Classify the preparation.
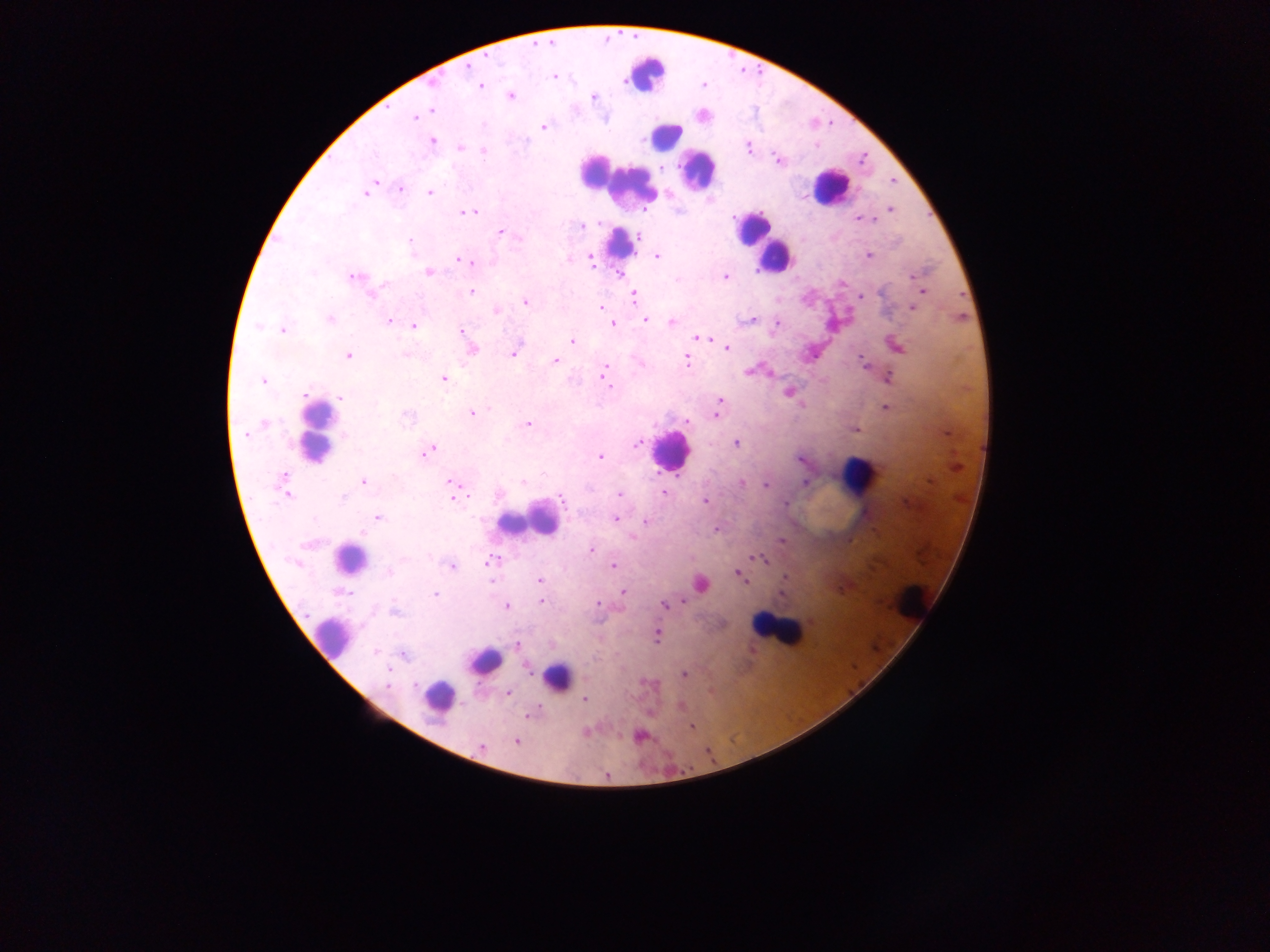

Thick blood smear.

Approximate centers as (x, y) in pixels.
Summary:
  - Malaria parasite locations: (487, 58), (467, 66), (554, 76), (624, 81), (434, 83), (704, 85), (480, 86), (510, 96), (594, 97), (431, 110), (420, 114), (415, 117), (543, 127), (433, 142), (460, 147), (748, 148), (483, 150), (777, 160), (663, 168), (893, 181), (401, 189), (366, 193), (430, 193), (891, 210), (470, 213), (866, 219), (582, 226), (500, 232), (639, 235), (519, 237), (410, 241), (657, 255), (868, 256), (590, 259), (458, 260), (471, 263), (429, 272), (621, 274), (915, 276), (353, 277), (724, 277), (677, 279), (384, 285), (380, 288), (922, 291), (471, 292), (860, 296), (370, 297), (634, 297), (525, 302), (912, 307), (601, 308), (497, 311), (330, 319), (645, 319), (753, 319), (388, 321), (672, 322), (612, 323), (776, 323), (414, 325), (258, 326), (282, 330), (462, 331), (697, 338), (705, 338), (572, 341), (897, 347), (726, 348), (473, 349), (514, 354), (347, 355), (404, 355), (862, 358), (556, 360), (686, 360), (606, 368), (748, 371), (604, 373), (888, 378), (443, 379), (263, 381), (607, 381), (789, 392), (305, 395), (341, 397), (719, 401), (886, 407), (472, 413), (716, 416), (407, 418), (687, 421), (528, 424), (856, 429), (245, 435), (637, 442), (736, 444), (429, 451), (600, 457), (800, 460), (282, 477), (364, 482), (451, 482), (523, 482), (806, 482), (742, 483), (765, 486), (663, 493), (619, 494), (287, 495), (454, 498), (342, 499), (563, 500), (705, 501), (785, 503), (378, 517), (615, 519), (645, 521), (716, 530), (363, 532), (781, 541), (591, 550), (762, 559), (491, 562), (613, 565), (451, 566), (389, 572), (739, 573), (786, 577), (540, 579), (701, 584), (624, 591), (782, 594), (434, 595), (542, 601), (597, 603), (665, 604), (507, 606), (395, 611), (657, 635), (516, 644), (375, 652), (403, 655), (684, 675), (388, 686), (509, 692), (585, 699), (680, 706), (537, 709), (531, 714), (692, 727), (638, 737), (516, 741), (481, 747), (606, 776)
  - Leukocyte locations: (648, 73), (665, 137), (697, 169), (617, 183), (830, 188), (753, 229), (621, 244), (773, 256), (317, 433), (670, 451), (859, 476), (530, 520), (348, 558), (913, 599), (775, 631), (331, 636), (485, 660), (557, 677), (439, 696)
  - Country: Ghana
  - Image size: 1270×952 pixels
  - Field of view: single
  - Capture: mobile-phone photograph through a microscope